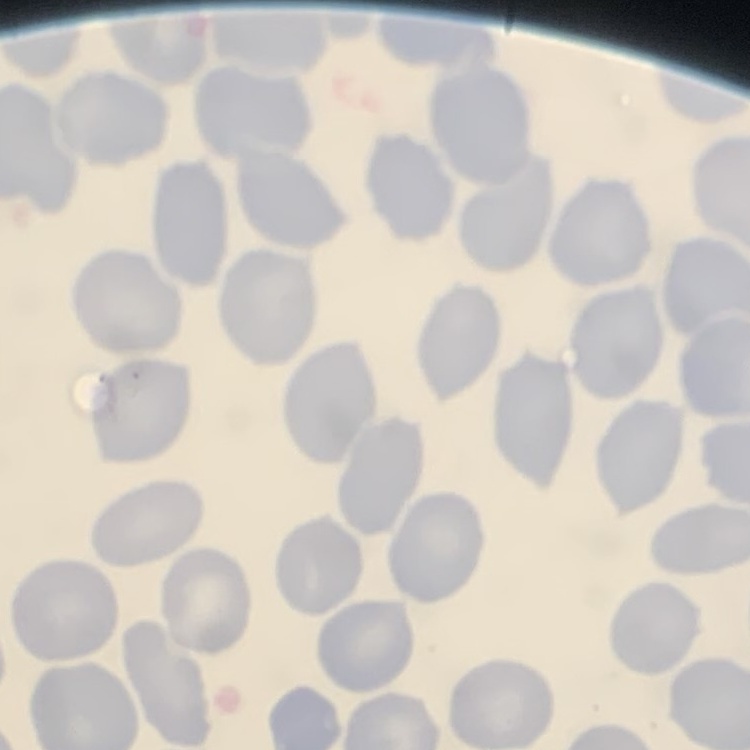

The red blood cells show no rouleaux formation. Stained with either Field's or Giemsa. One tile cut from a larger photomicrograph. Thin peripheral smear.